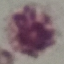

Summary:
  - Malaria status: uninfected
  - Image type: cell patch, automatically extracted from a larger field of view and resized to 64 × 64 pixels
  - Preparation: thin smear
  - Stain: Giemsa
  - Capture: smartphone through the microscope eyepiece